Assess this cell for malaria.
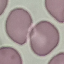
It is uninfected.

Giemsa-stained preparation. Thin blood film. Photographed with a smartphone camera at the microscope eyepiece. Automatically extracted cell patch, resized to 64 × 64 pixels.